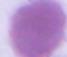
Summary:
  - Magnification: 1000x
  - Identification: red blood cell
  - Modality: micrograph